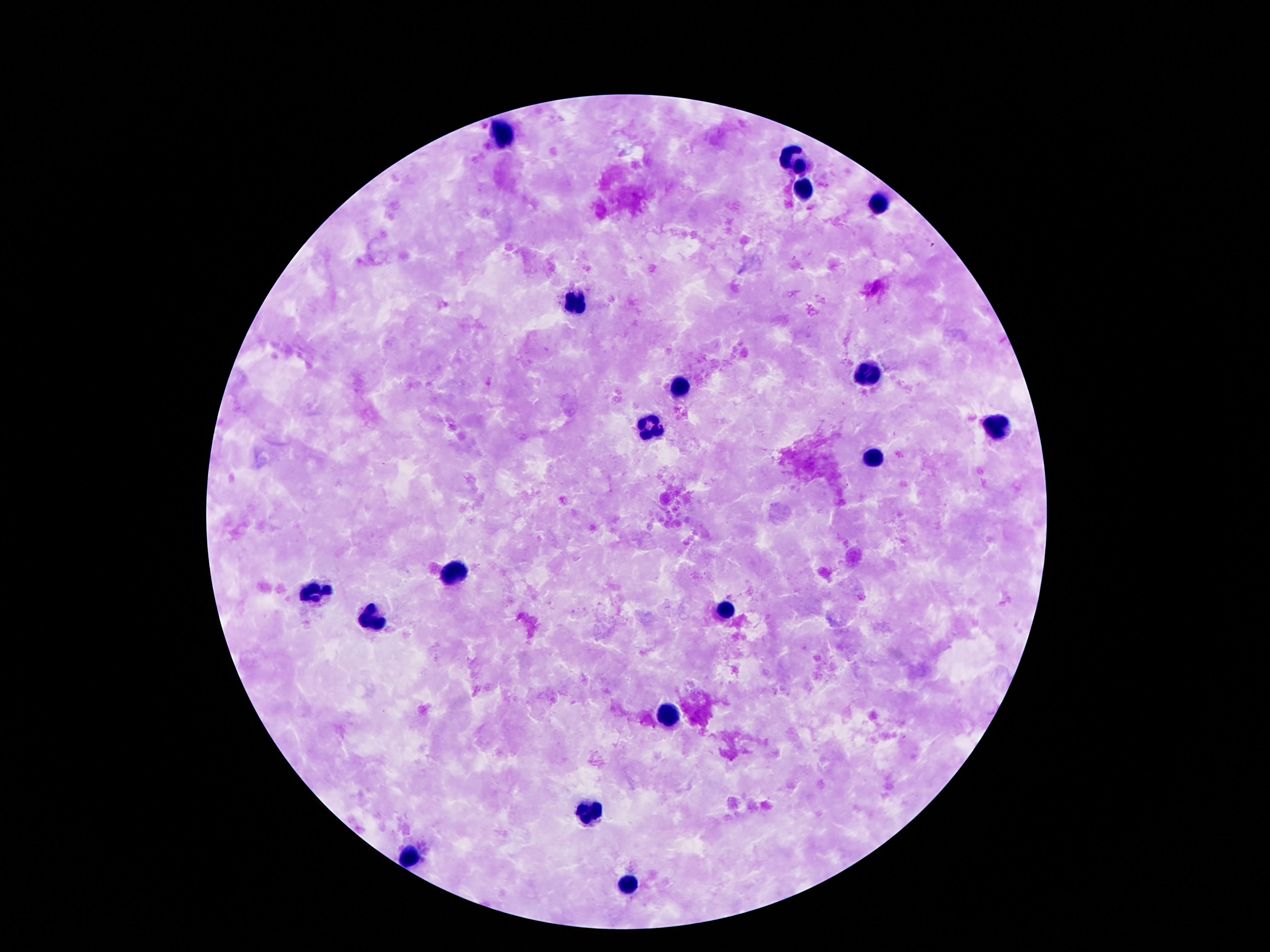
Approximate centers as [x, y] in pixels.
Summary:
  - Leukocyte locations: [506, 135], [798, 160], [804, 190], [880, 201], [574, 305], [870, 368], [682, 385], [648, 431], [990, 431], [872, 456], [458, 571], [314, 593], [722, 609], [370, 619], [668, 715], [588, 814], [416, 857], [632, 886]
  - Image size: 1270×952 pixels
  - Capture: smartphone camera through the microscope eyepiece
  - Magnification: 100x
  - Patient malaria status: not infected
  - Preparation: thick blood film
  - Field of view: one from this slide
  - Stain: Giemsa